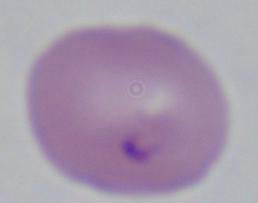

modality = photomicrograph
magnification = 1000x
identification = Babesia